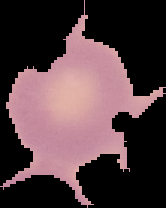
From a thin blood film. Result: no Plasmodium parasites detected. The area outside the segmented cell region is set to black. Image is 166×208 pixels.